State which parasite is depicted.
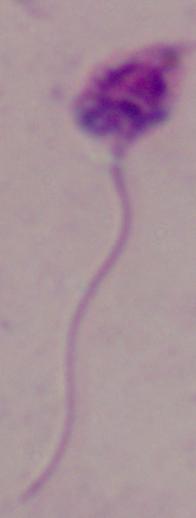

Leishmania.

Summary:
  - Modality: photomicrograph
  - Magnification: 1000x